Locate every leukocyte (white blood cell).
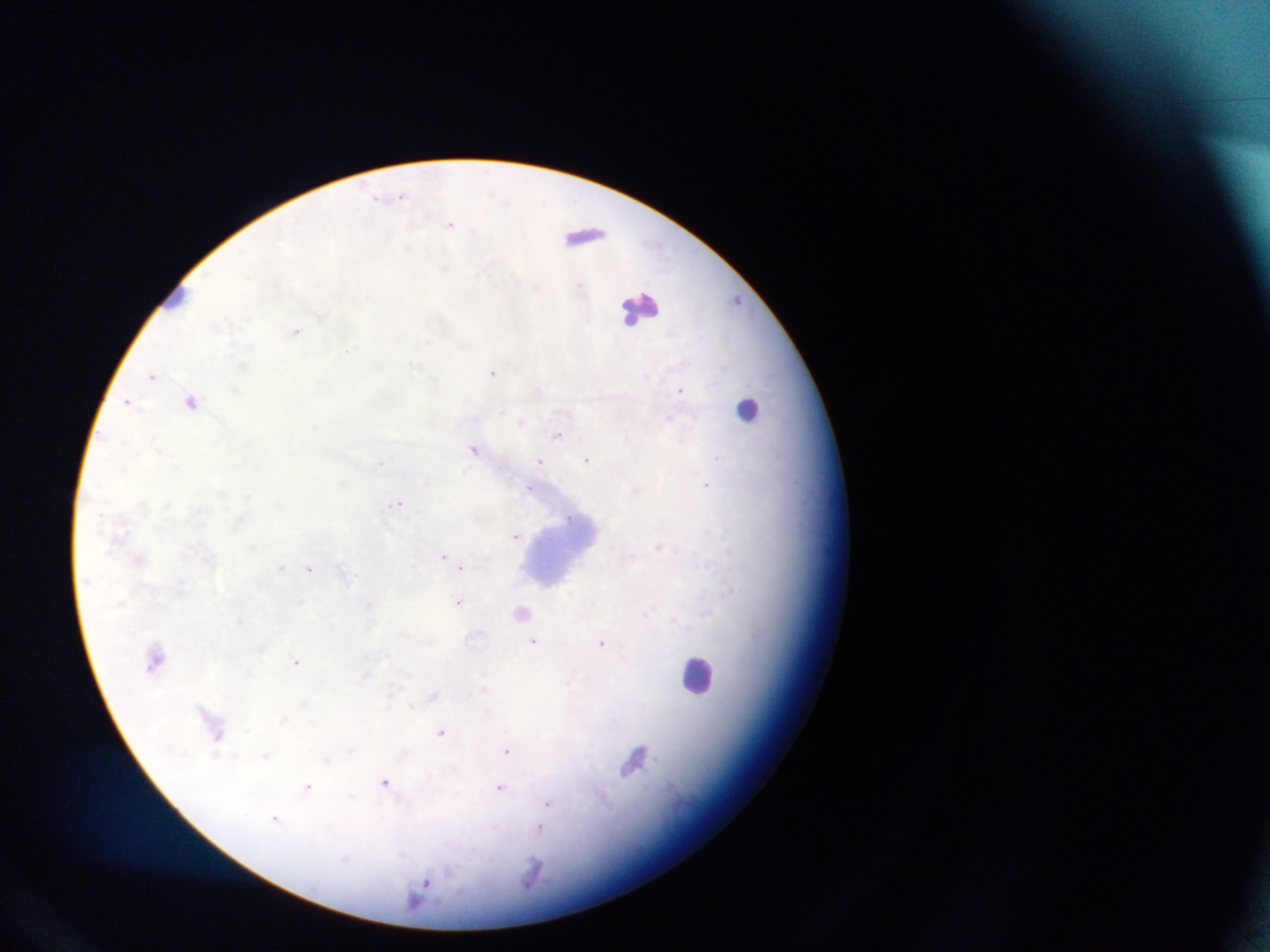
Approximate centers as [x, y] in pixels.
Leukocytes: [585, 231], [179, 304], [638, 312], [751, 409], [696, 672].

Summary:
  - Plasmodium parasite locations: [375, 194], [401, 195], [449, 225], [472, 230], [736, 298], [153, 373], [492, 373], [680, 391], [128, 400], [192, 401], [521, 421], [558, 434], [472, 448], [719, 457], [587, 458], [541, 461], [706, 485], [527, 487], [398, 502], [517, 535], [442, 556], [463, 566], [310, 568], [458, 602], [534, 640], [601, 643], [296, 660], [483, 689], [434, 694], [411, 705], [441, 733], [507, 749], [386, 782], [308, 787], [501, 788], [549, 802], [276, 819], [542, 827], [425, 885]
  - Field of view: single
  - Preparation: thick blood smear
  - Image size: 1270×952 pixels
  - Country: Ghana
  - Capture: mobile-phone photograph through a microscope